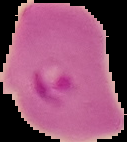

preparation: thin blood film
malaria_status: parasitized
image_size: 127×142 pixels
image_type: segmented cell region on a black background